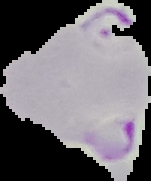
{
  "preparation": "thin blood film",
  "image_type": "segmented cell region on a black background",
  "malaria_status": "parasitized",
  "image_size": "151×181 pixels"
}